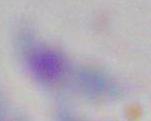

Summary:
  - Modality: photomicrograph
  - Identification: Toxoplasma gondii
  - Magnification: 1000x